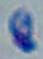
Summary:
  - Modality: photomicrograph
  - Identification: Toxoplasma gondii
  - Magnification: 1000x